Assess this cell for malaria.
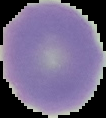

Uninfected.

Summary:
  - Image size: 106×118 pixels
  - Preparation: thin blood smear
  - Image type: cell region segmented out of the field of view; surrounding area masked to black